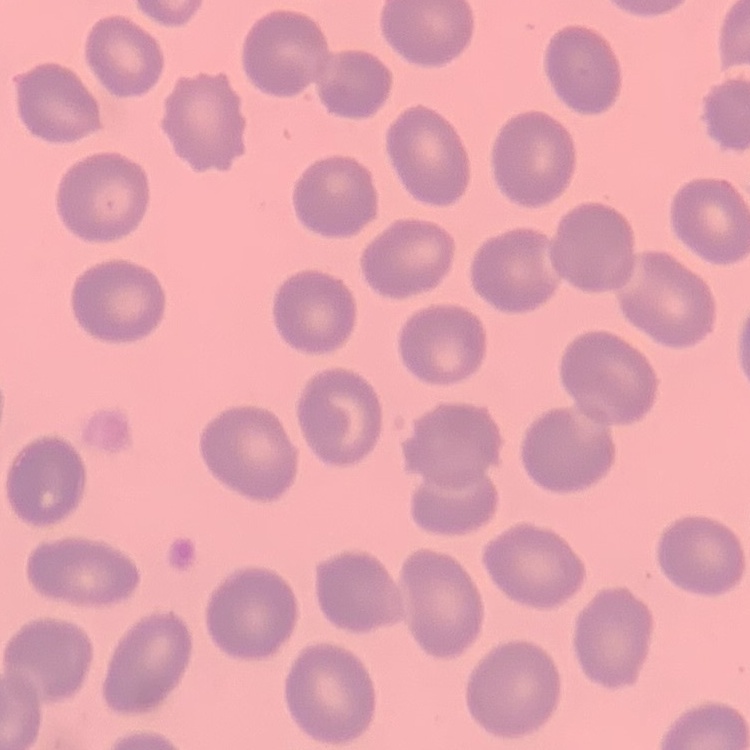

erythrocyte morphology = no rouleaux formation
image type = square crop of a larger photomicrograph
preparation = thin blood film
stain = Field's or Giemsa